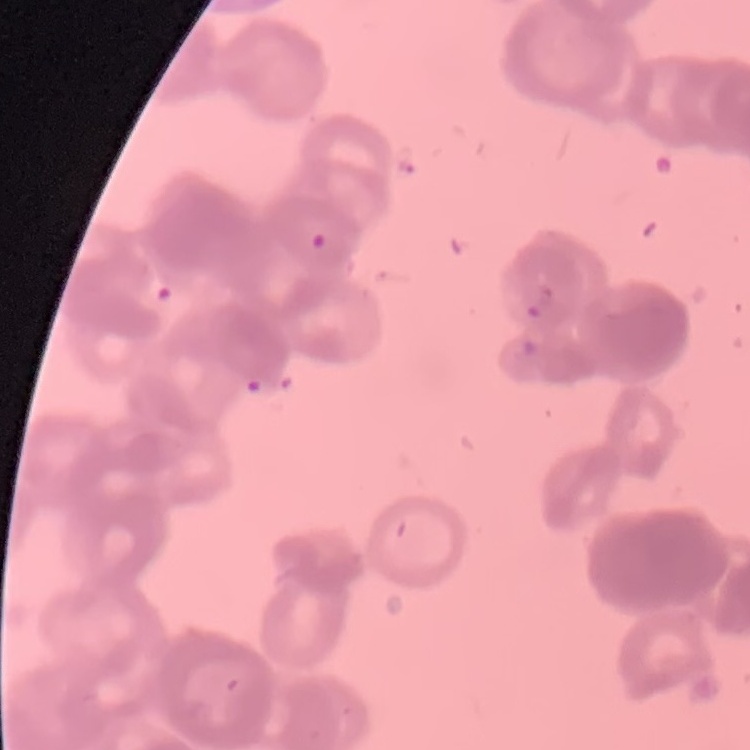

Summary:
  - Red blood cell morphology: rouleaux formation
  - Preparation: thin blood smear
  - Stain: Field's or Giemsa
  - Image type: square crop of a larger photomicrograph